Report the malaria status of this cell.
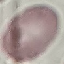

It is uninfected.

Summary:
  - Capture: smartphone through the microscope eyepiece
  - Preparation: thin smear
  - Image type: automatically extracted cell patch, resized to 64 × 64 pixels
  - Stain: Giemsa